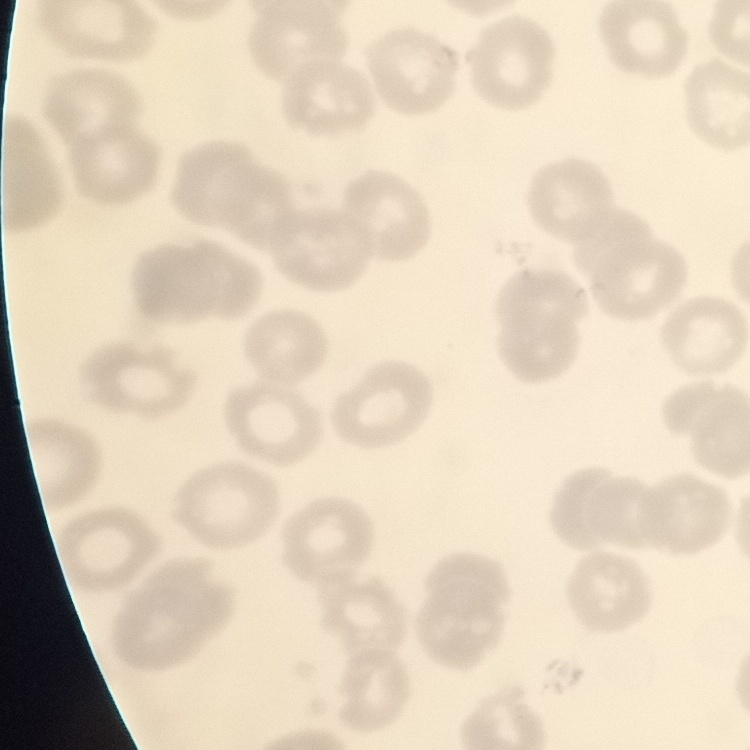 The red blood cells exhibit no rouleaux formation. Thin peripheral smear. Field's or Giemsa stain. Square crop of a larger photomicrograph.